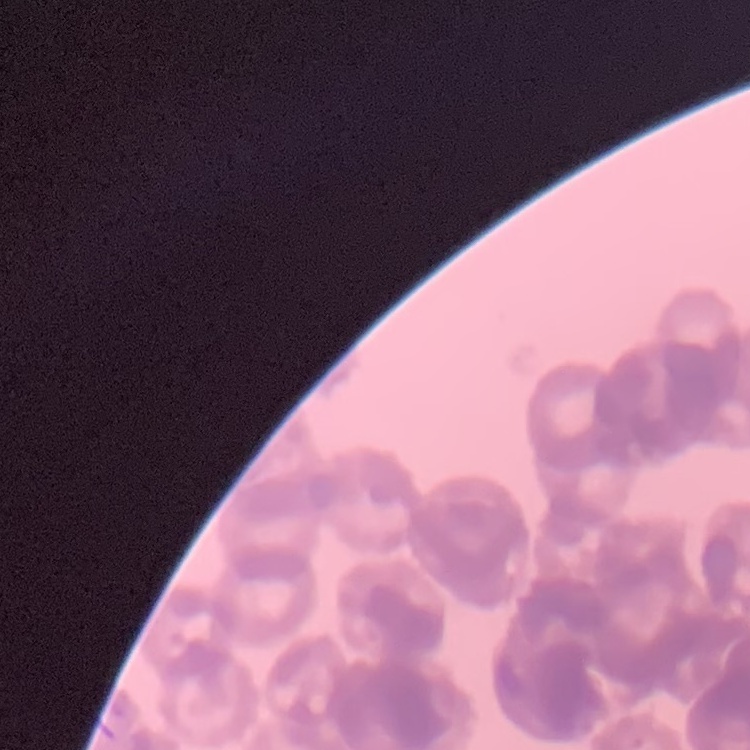 The red blood cells show rouleaux formation. Stained with either Field's or Giemsa. Thin blood film. Square crop of a larger photomicrograph.